Identify the cell.
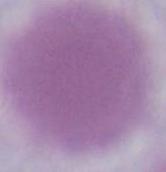

An erythrocyte.

modality = micrograph
magnification = 1000x